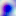
{
  "modality": "photomicrograph",
  "magnification": "400x",
  "identification": "Toxoplasma gondii"
}